Assess this cell for malaria.
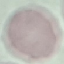

Uninfected.

Summary:
  - Image type: cell patch, automatically extracted from a larger field of view and resized to 64 × 64 pixels
  - Capture: smartphone through the microscope eyepiece
  - Preparation: thin blood smear
  - Stain: Giemsa